Locate every blood parasite and identify its species.
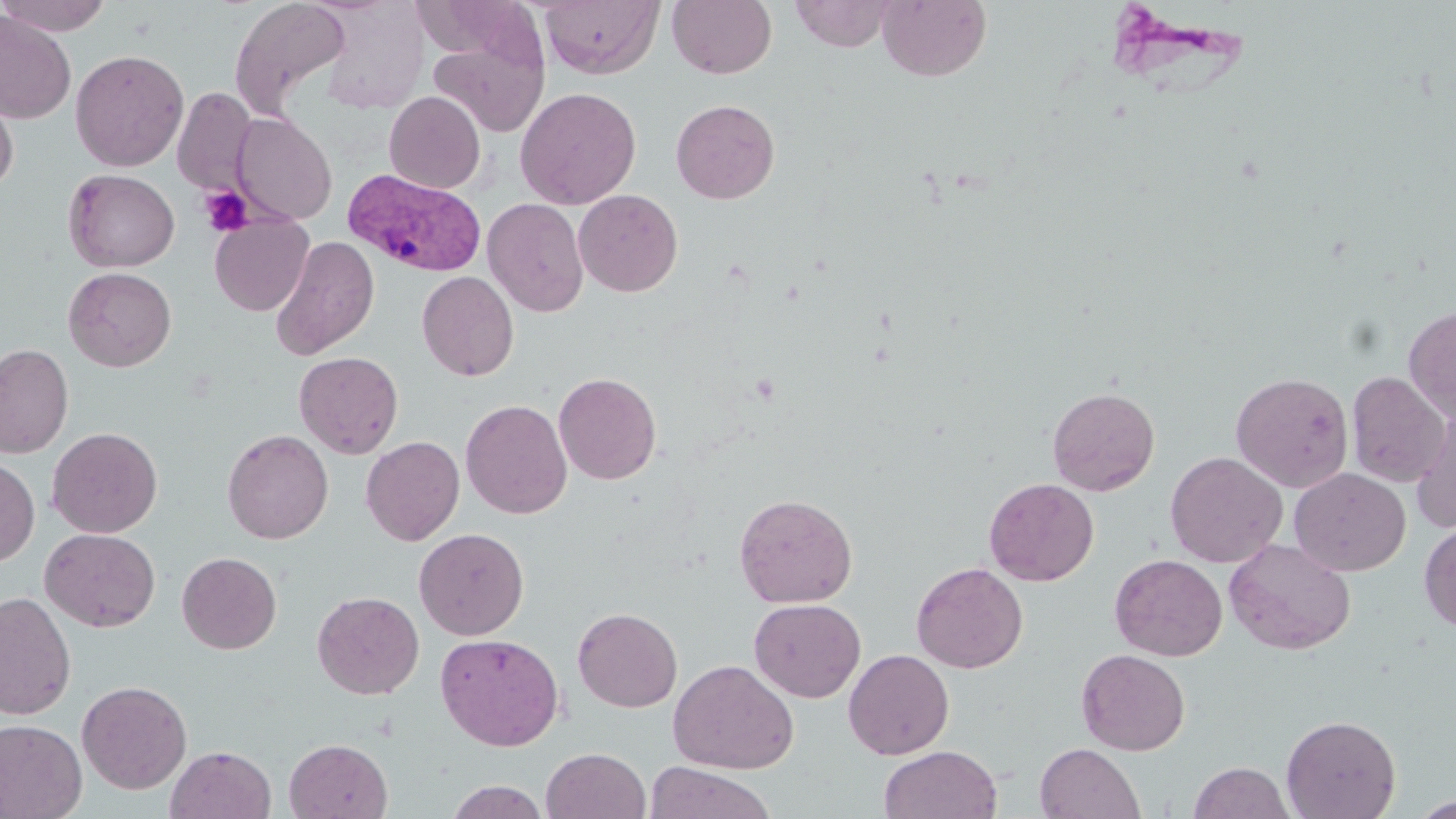
Approximate bounding boxes as (x1, y1, x2, y2) in pixels.
Plasmodium vivax-infected red blood cells: (344, 168, 486, 276).
No Plasmodium falciparum, Plasmodium ovale, Plasmodium malariae, Babesia divergens, or Trypanosoma brucei observed.

slide-level diagnosis = Plasmodium vivax
platelet locations = approximate bounding boxes as (x1, y1, x2, y2) in pixels: (199, 185, 254, 236)
field of view = one of a larger specimen
stain = May-Grünwald-Giemsa
uninfected red blood cell locations = approximate bounding boxes as (x1, y1, x2, y2) in pixels: (0, 0, 115, 36), (229, 0, 352, 118), (408, 0, 539, 64), (539, 0, 664, 79), (668, 0, 777, 79), (789, 0, 897, 52), (878, 0, 991, 82), (0, 11, 77, 124), (430, 37, 547, 136), (70, 48, 189, 171), (0, 86, 18, 195), (515, 86, 641, 209), (172, 88, 256, 195), (384, 91, 486, 193), (671, 99, 780, 203), (231, 113, 337, 224), (63, 169, 179, 272), (574, 189, 683, 297), (483, 198, 589, 317), (209, 214, 313, 316), (270, 235, 379, 360), (63, 267, 177, 372), (417, 271, 519, 381), (1403, 305, 1456, 423), (0, 343, 73, 458), (294, 351, 403, 459), (1231, 371, 1353, 492), (1347, 371, 1451, 487), (553, 372, 662, 484), (1047, 386, 1160, 496), (460, 399, 572, 519), (1412, 402, 1456, 532), (47, 427, 163, 537), (222, 428, 334, 544), (361, 436, 465, 545), (1165, 451, 1288, 568), (0, 458, 39, 567), (1289, 467, 1410, 576), (984, 477, 1099, 586), (734, 493, 858, 608), (1419, 521, 1456, 633), (413, 527, 529, 640), (40, 528, 160, 632), (1223, 538, 1357, 654), (177, 552, 281, 654), (1110, 554, 1228, 661), (911, 562, 1028, 674), (0, 591, 77, 721), (312, 591, 424, 699), (749, 598, 865, 702), (572, 607, 682, 712), (435, 633, 564, 751), (1076, 648, 1191, 755), (843, 649, 954, 759), (668, 659, 799, 774), (77, 680, 192, 794), (1281, 714, 1401, 819), (0, 719, 87, 819), (284, 738, 393, 819), (1035, 743, 1146, 819), (166, 745, 276, 819), (879, 745, 1002, 819), (542, 748, 651, 819), (644, 761, 775, 819), (1188, 762, 1295, 819), (444, 780, 551, 819), (1411, 796, 1456, 818)
modality = optical microscopy
image size = 1456×819 pixels
preparation = thin blood film
magnification = 1000x